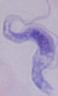 1000x magnification. A trypanosome is shown. Photomicrograph.